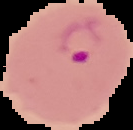 The area outside the segmented cell region is set to black. From a thin blood film. Result: Plasmodium parasites detected. Image is 133×130 pixels.